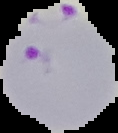
From a thin blood film. Malaria status: parasitized. Image is 118×133 pixels. Cell region segmented out of the field of view; the surrounding area is masked to black.